Mark where leukocytes are.
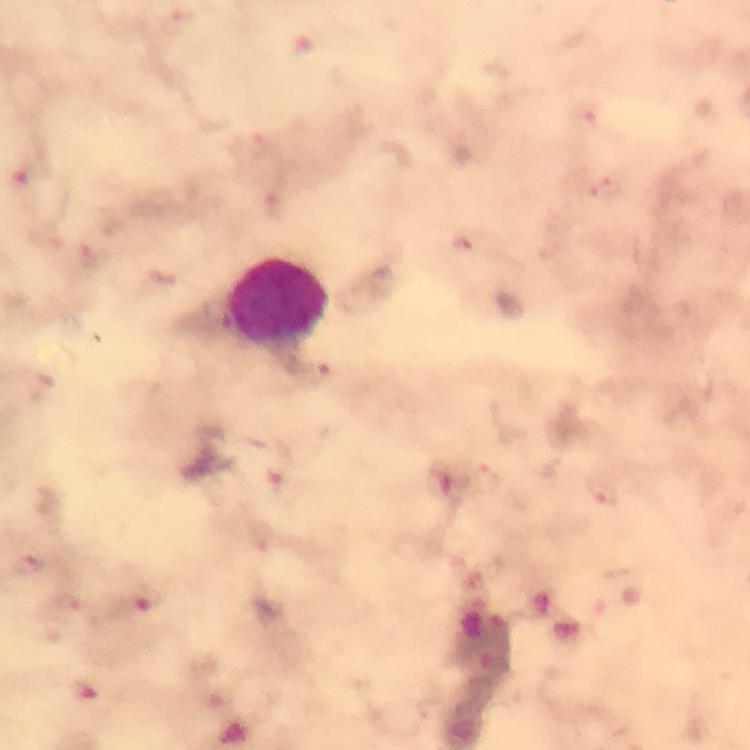

Approximate centers as [x, y] in pixels.
Leukocytes: [279, 304].

Summary:
  - Malaria parasite locations: [607, 188], [276, 473], [488, 477], [604, 492], [28, 564], [146, 594]
  - Immersion oil: used
  - Context: from a malaria diagnostic workup
  - Stain: Giemsa
  - Magnification: 100x
  - Capture: smartphone photograph through a microscope
  - Cropped from: a single field of view
  - Preparation: thick blood film
  - Image size: 750×750 pixels